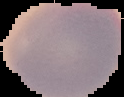

image_type: cell region segmented out of the field of view; surrounding area masked to black
result: negative for malaria parasites
image_size: 124×97 pixels
preparation: thin blood smear